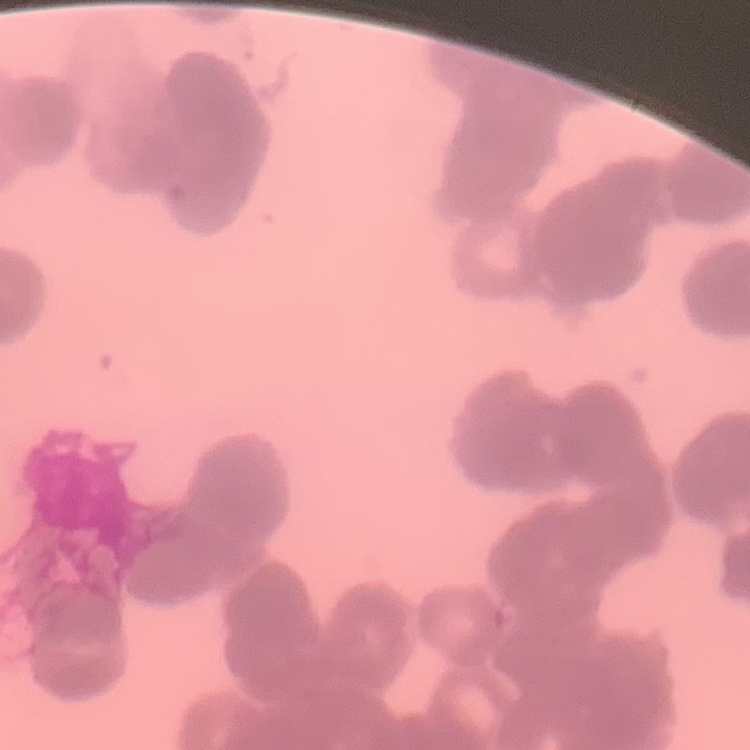

red_blood_cell_morphology: rouleaux formation
image_type: square crop of a larger photomicrograph
stain: Field's or Giemsa
preparation: thin peripheral smear